Locate every leukocyte (white blood cell).
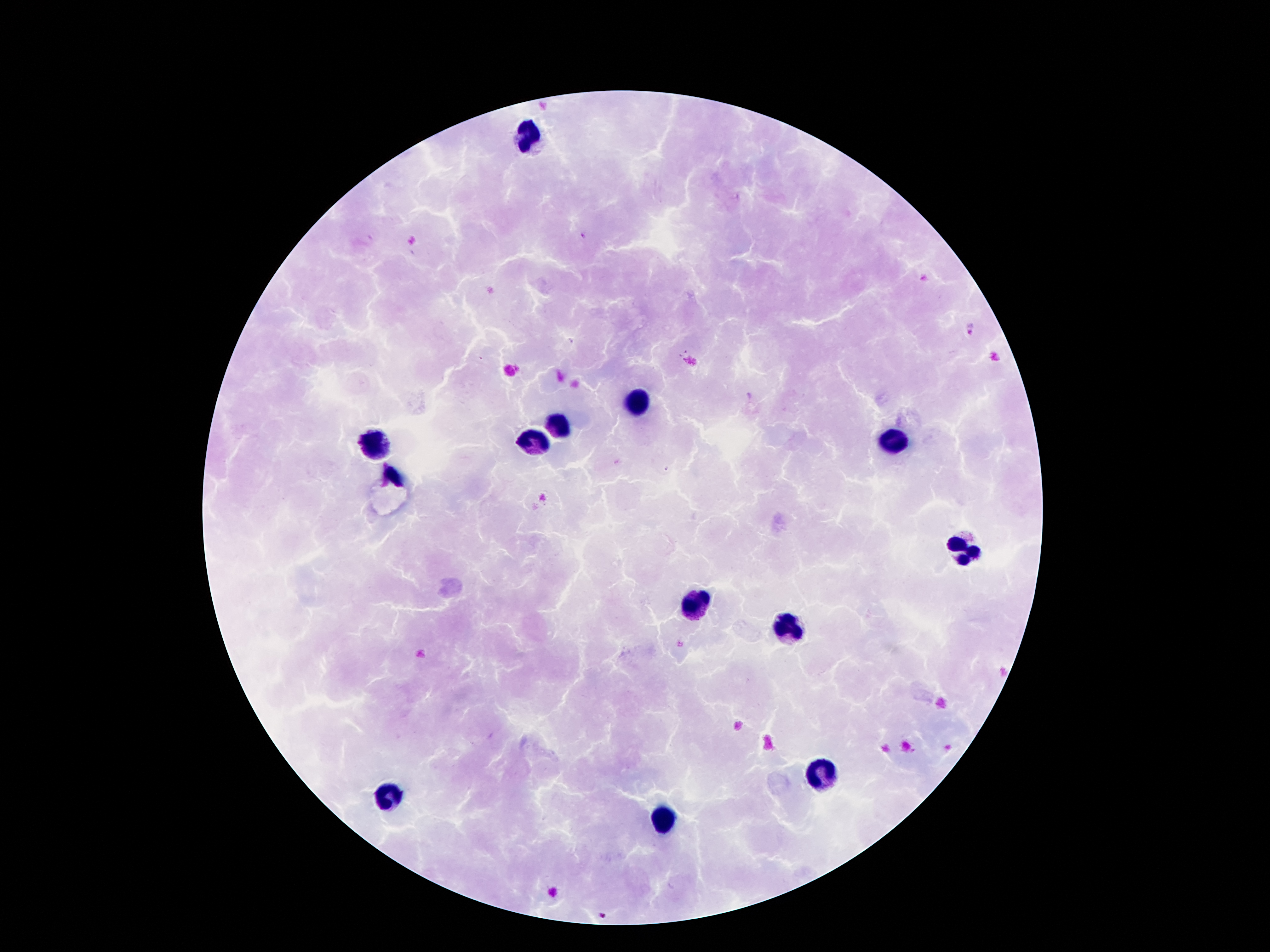

Approximate centers as [x, y] in pixels.
Leukocytes: [530, 135], [637, 400], [555, 429], [532, 440], [374, 442], [891, 446], [391, 476], [964, 549], [698, 604], [787, 626], [818, 772], [390, 795], [664, 817].

Malaria parasite locations: [585, 236], [971, 327], [602, 916]. Thick blood smear. Giemsa stain. Smartphone photograph taken through the microscope eyepiece. Patient malaria status: positive for Plasmodium falciparum. 100x magnification. One field from this slide. Image is 1270×952 pixels.